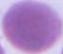
Summary:
  - Modality: photomicrograph
  - Magnification: 1000x
  - Identification: red blood cell